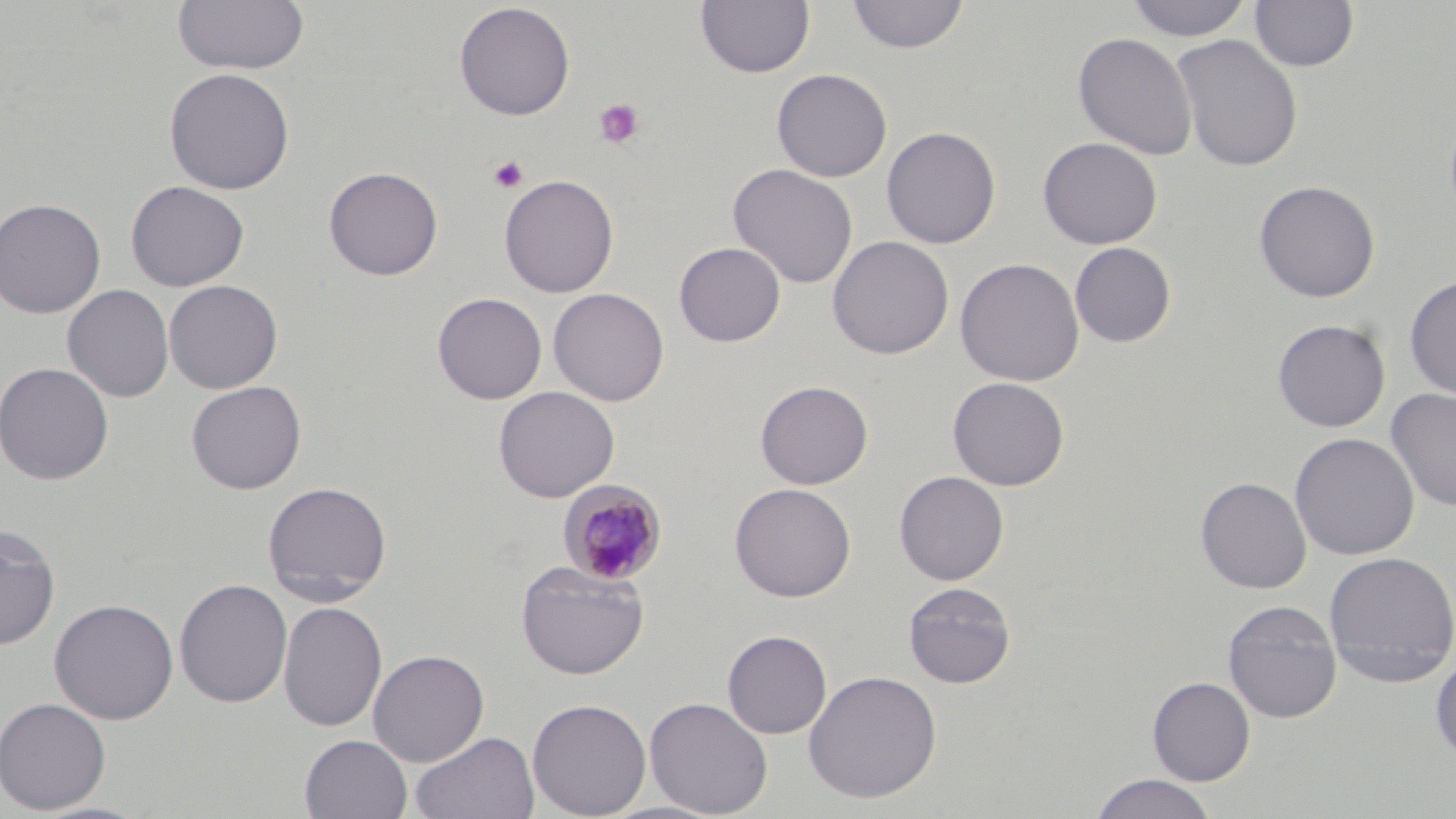
Summary:
  - Coordinate format: approximate bounding boxes as (x1,y1)-(x2,y2) corner pairs in pixels
  - Uninfected red blood cell locations: (696,0)-(815,79), (847,0)-(970,54), (1124,0)-(1253,42), (1249,0)-(1359,72), (171,1)-(310,75), (453,2)-(575,120), (1073,32)-(1197,161), (1170,33)-(1304,172), (164,67)-(295,195), (772,68)-(893,182), (881,126)-(1001,249), (1038,136)-(1162,249), (728,164)-(858,289), (323,166)-(444,281), (499,174)-(619,298), (125,180)-(250,291), (1254,180)-(1380,303), (0,198)-(106,319), (827,235)-(954,360), (674,242)-(786,347), (1069,242)-(1176,347), (954,257)-(1085,387), (1403,276)-(1456,400), (164,279)-(283,394), (62,284)-(174,402), (548,288)-(670,406), (432,292)-(547,404), (1272,318)-(1390,432), (0,361)-(114,485), (947,377)-(1070,490), (186,380)-(307,494), (755,380)-(874,489), (493,386)-(620,502), (1385,387)-(1456,512), (1289,432)-(1419,561), (894,470)-(1009,585), (1195,476)-(1311,594), (262,480)-(392,603), (730,482)-(856,602), (0,524)-(60,651), (1323,550)-(1456,687), (515,560)-(650,680), (174,578)-(292,708), (902,581)-(1017,689), (49,598)-(179,724), (1222,600)-(1342,723), (278,601)-(387,732), (722,630)-(832,738), (368,649)-(489,765), (1430,651)-(1456,764), (803,669)-(942,804), (1147,676)-(1255,786), (645,696)-(773,817), (0,697)-(112,814), (527,698)-(652,818), (410,730)-(539,819), (299,734)-(412,819), (1089,773)-(1218,818)
  - Platelet locations: (593,97)-(646,150), (489,155)-(529,192)
  - Plasmodium malariae-infected red blood cell locations: (558,479)-(667,586)
  - Slide-level diagnosis: Plasmodium malariae
  - Preparation: thin blood smear
  - Magnification: 1000x
  - Modality: light microscopy
  - Stain: May-Grünwald-Giemsa
  - Image size: 1456×819 pixels
  - Field of view: single